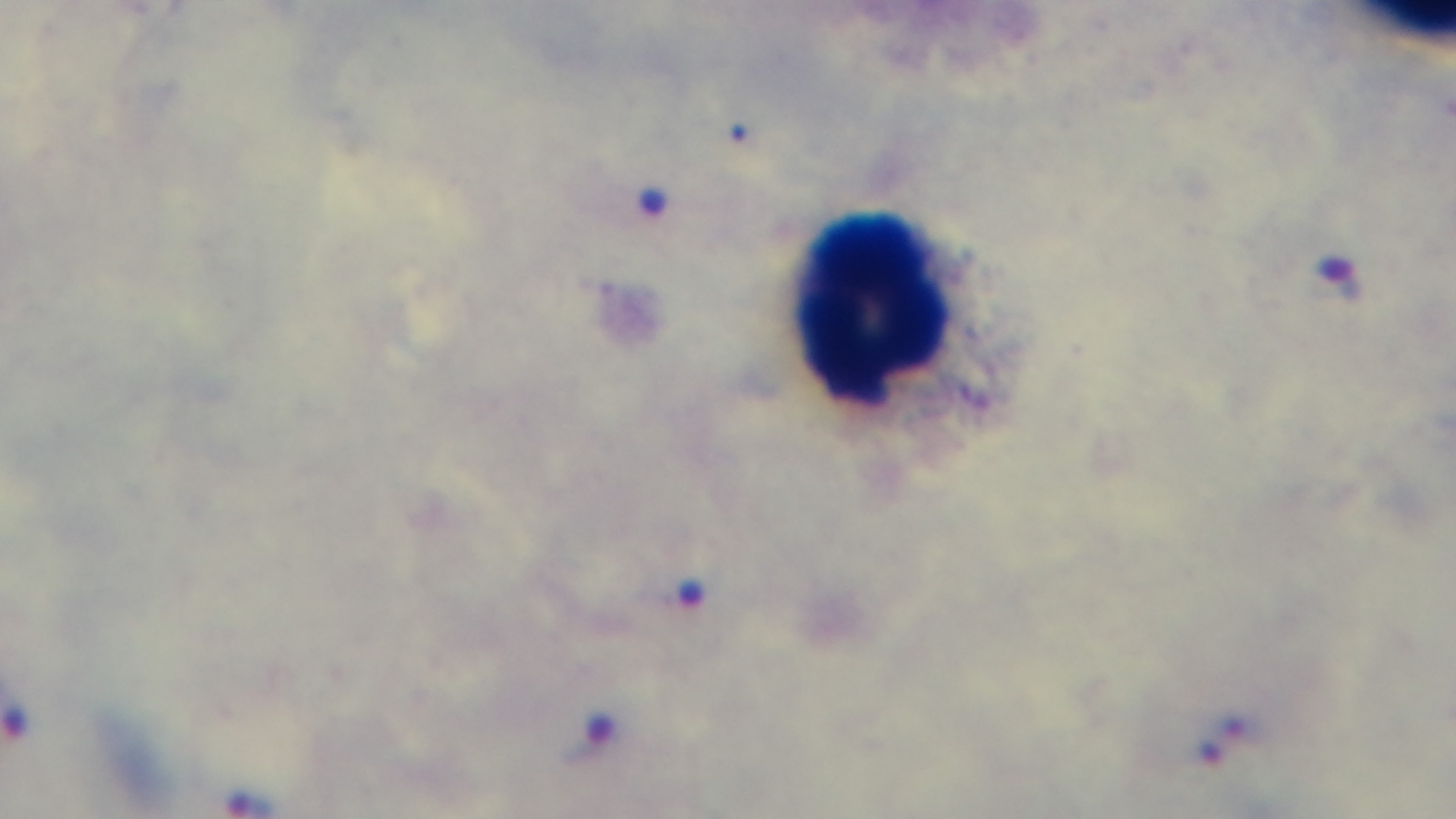

field of view = single
stain = Giemsa
malaria status = infected
capture = mounted 4K digital camera
modality = light microscopy
preparation = thick
objective = 100x oil immersion